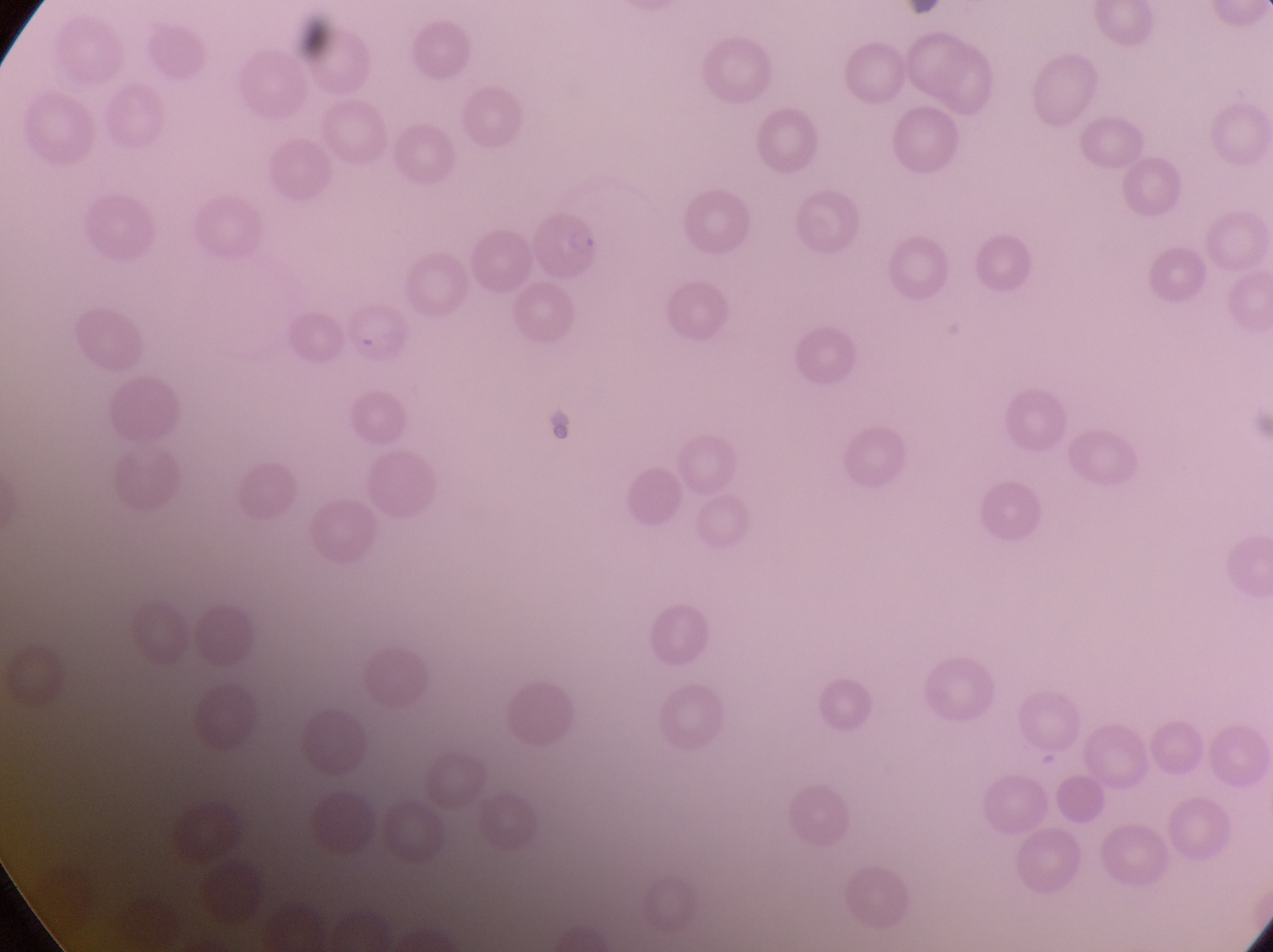
Approximate bounding boxes as [left, top, right, bottom] in pixels. Parasitised red blood cell locations: [526, 210, 606, 292], [338, 299, 418, 372]. Photographed through the eyepiece of an Olympus CX-23 microscope with a smartphone camera. Thin blood film. At a magnification of 1000x. Image is 1273×952 pixels. Sample from Uganda. Single field of view.